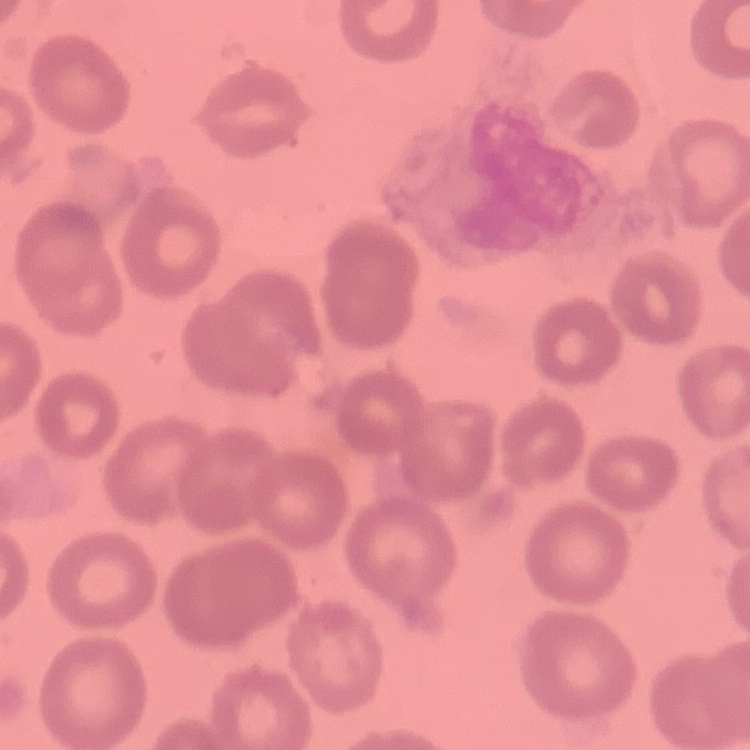

Summary:
  - Erythrocyte morphology: no rouleaux formation
  - Stain: Field's or Giemsa
  - Image type: one tile cut from a larger photomicrograph
  - Preparation: thin blood smear